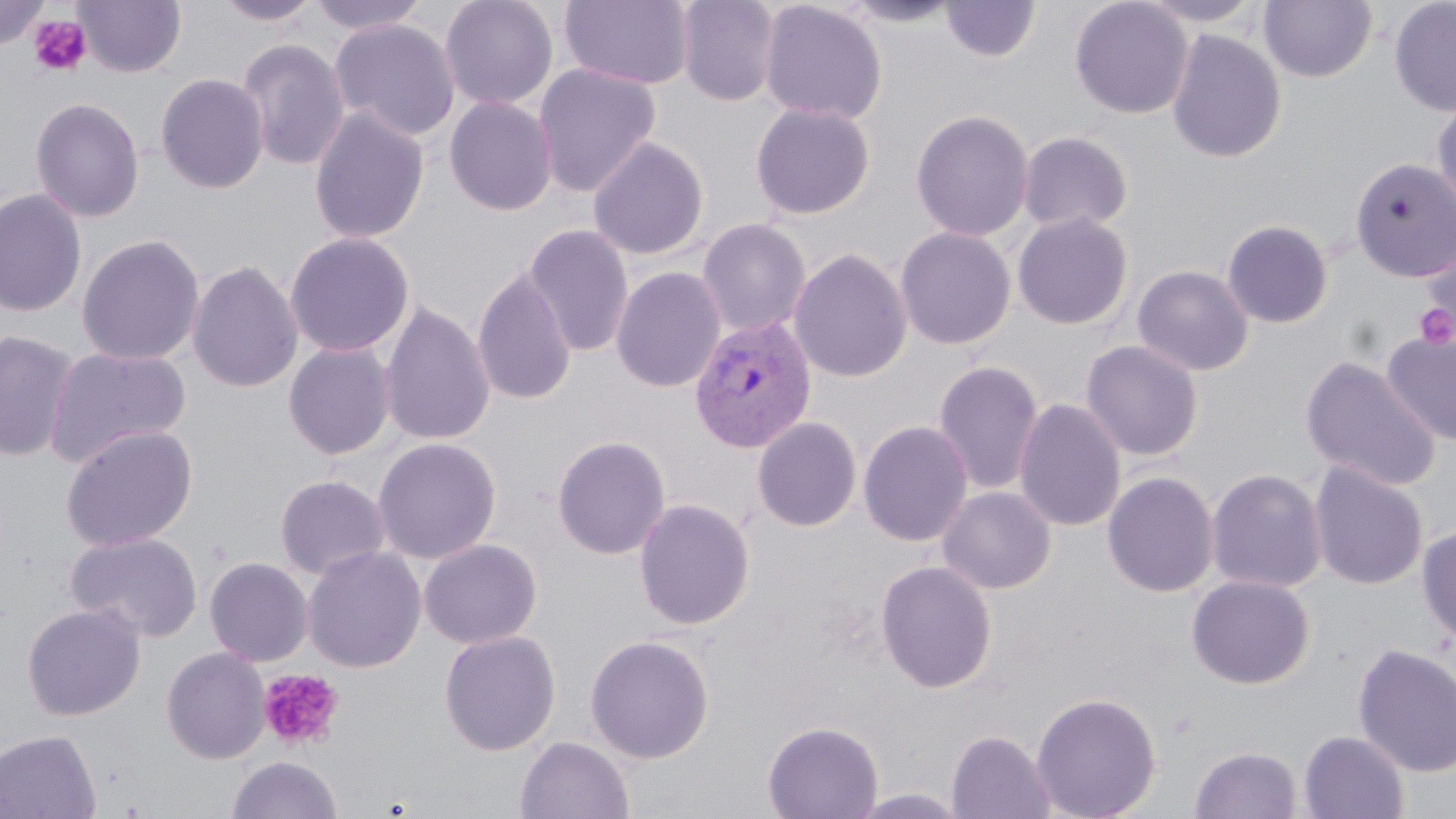
Plasmodium vivax-infected red blood cell locations = approximate bounding boxes as (x1,y1)-(x2,y2) corner pairs in pixels: (688,315)-(818,453)
slide-level diagnosis = Plasmodium vivax
image size = 1456×819 pixels
uninfected red blood cell locations = approximate bounding boxes as (x1,y1)-(x2,y2) corner pairs in pixels: (0,0)-(50,52), (74,0)-(186,78), (214,0)-(325,27), (305,0)-(432,36), (439,0)-(559,110), (559,0)-(695,91), (675,0)-(781,107), (759,0)-(888,124), (839,0)-(965,29), (1070,0)-(1193,119), (1134,0)-(1267,28), (1259,0)-(1377,82), (1389,0)-(1456,117), (940,1)-(1041,63), (329,19)-(461,141), (1166,29)-(1287,164), (237,37)-(351,172), (533,63)-(662,198), (155,73)-(270,194), (1430,95)-(1456,218), (444,96)-(558,216), (30,97)-(145,223), (750,102)-(876,220), (308,107)-(430,244), (910,109)-(1034,241), (1017,131)-(1133,235), (588,136)-(709,260), (1350,157)-(1456,282), (0,188)-(87,318), (1012,212)-(1133,330), (697,218)-(812,338), (1221,219)-(1334,329), (523,224)-(634,358), (895,226)-(1016,350), (284,232)-(414,357), (76,233)-(205,366), (1419,233)-(1456,345), (788,248)-(912,383), (187,260)-(303,394), (1132,265)-(1254,377), (611,266)-(726,394), (472,268)-(577,406), (379,302)-(496,446), (1382,328)-(1456,446), (0,330)-(80,462), (1080,339)-(1204,461), (283,342)-(396,460), (44,346)-(192,468), (1300,355)-(1443,491), (932,360)-(1044,496), (1013,397)-(1127,532), (751,416)-(863,532), (858,420)-(973,547), (60,424)-(199,551), (552,435)-(671,560), (372,437)-(501,563), (1308,461)-(1429,590), (1205,468)-(1328,594), (1101,471)-(1219,597), (275,474)-(391,581), (937,485)-(1056,595), (633,497)-(756,630), (1416,524)-(1456,647), (67,531)-(203,642), (418,538)-(543,649), (302,545)-(426,672), (204,556)-(313,667), (876,560)-(997,694), (1186,574)-(1316,689), (22,603)-(146,720), (439,630)-(561,755), (585,634)-(715,763), (1352,643)-(1456,778), (162,646)-(270,764), (1031,691)-(1162,819), (762,720)-(884,819), (0,729)-(101,819), (947,729)-(1055,819), (1298,730)-(1410,818), (515,735)-(635,819), (1189,746)-(1302,819), (227,755)-(343,819)
preparation = thin blood film
stain = May-Grünwald-Giemsa
field of view = one of a larger specimen
platelet locations = approximate bounding boxes as (x1,y1)-(x2,y2) corner pairs in pixels: (28,15)-(91,77), (1414,301)-(1455,352), (258,668)-(344,751)
magnification = 1000x
modality = optical microscopy